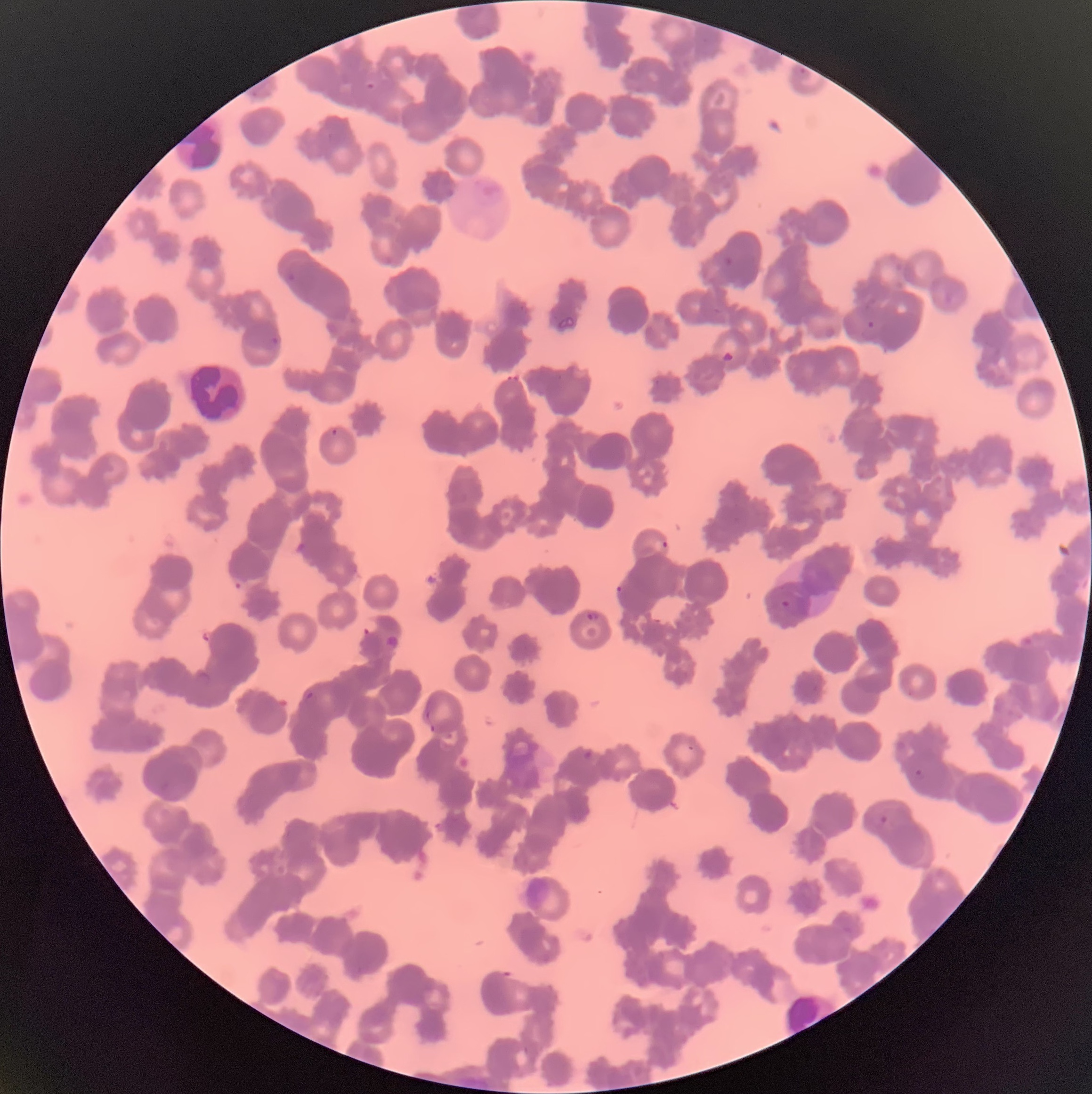

Approximate bounding boxes as (x1,y1)-(x2,y2) corner pairs in pixels. White blood cell locations: (188,358)-(246,424). Plasmodium parasite locations: (798,66)-(808,76), (364,81)-(376,91), (724,256)-(734,267), (285,272)-(298,284), (859,321)-(879,340), (269,335)-(280,347), (331,428)-(338,437), (652,538)-(669,553), (615,584)-(627,603), (781,599)-(791,609), (585,611)-(601,621), (195,670)-(211,686), (304,690)-(314,701), (425,699)-(433,720), (428,722)-(439,732), (581,749)-(594,761), (914,768)-(925,780), (878,815)-(889,825). The red blood cells show rouleaux formation. Thin blood film. Image is 1092×1094 pixels. Light microscopy.